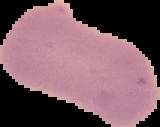
{
  "malaria_status": "uninfected",
  "preparation": "thin blood film",
  "image_type": "segmented cell region with the area outside set to black",
  "image_size": "160×127 pixels"
}